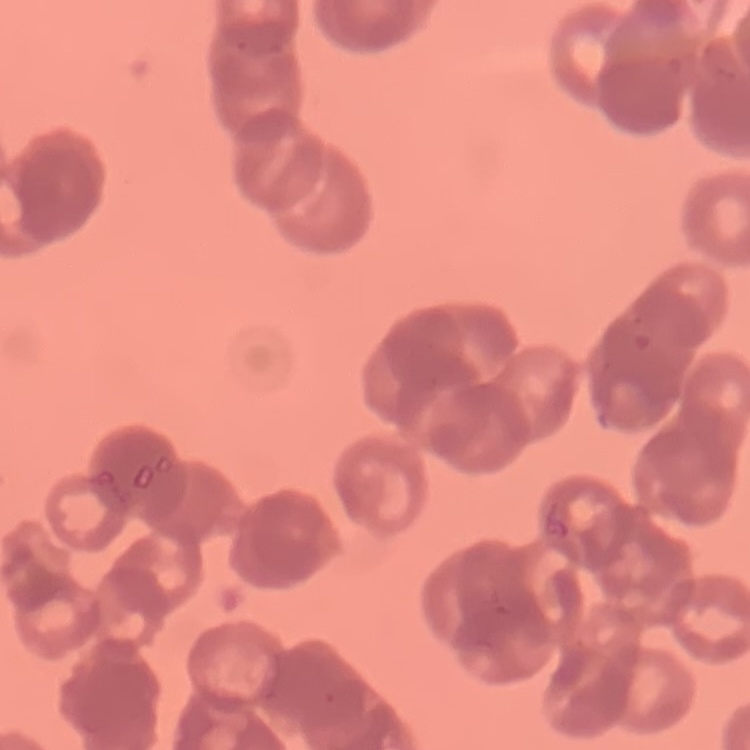
red blood cell morphology = rouleaux formation
stain = Field's or Giemsa
image type = square crop of a larger photomicrograph
preparation = thin blood film